Assess the morphology of the red blood cells.
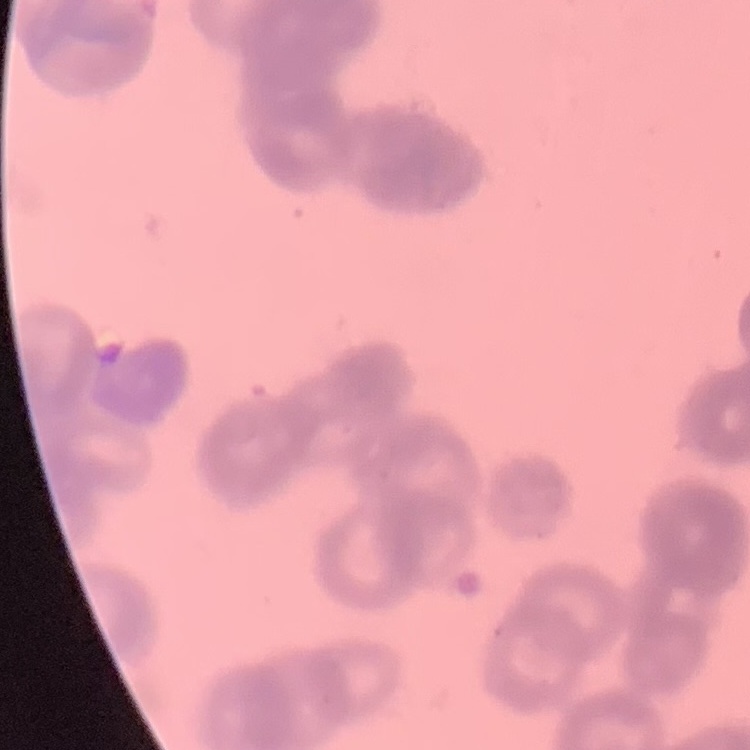

Rouleaux formation.

Field's or Giemsa stain. Thin blood smear. One tile cut from a larger photomicrograph.